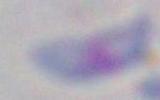
Summary:
  - Magnification: 1000x
  - Modality: micrograph
  - Identification: Toxoplasma gondii